Point out each Plasmodium parasite.
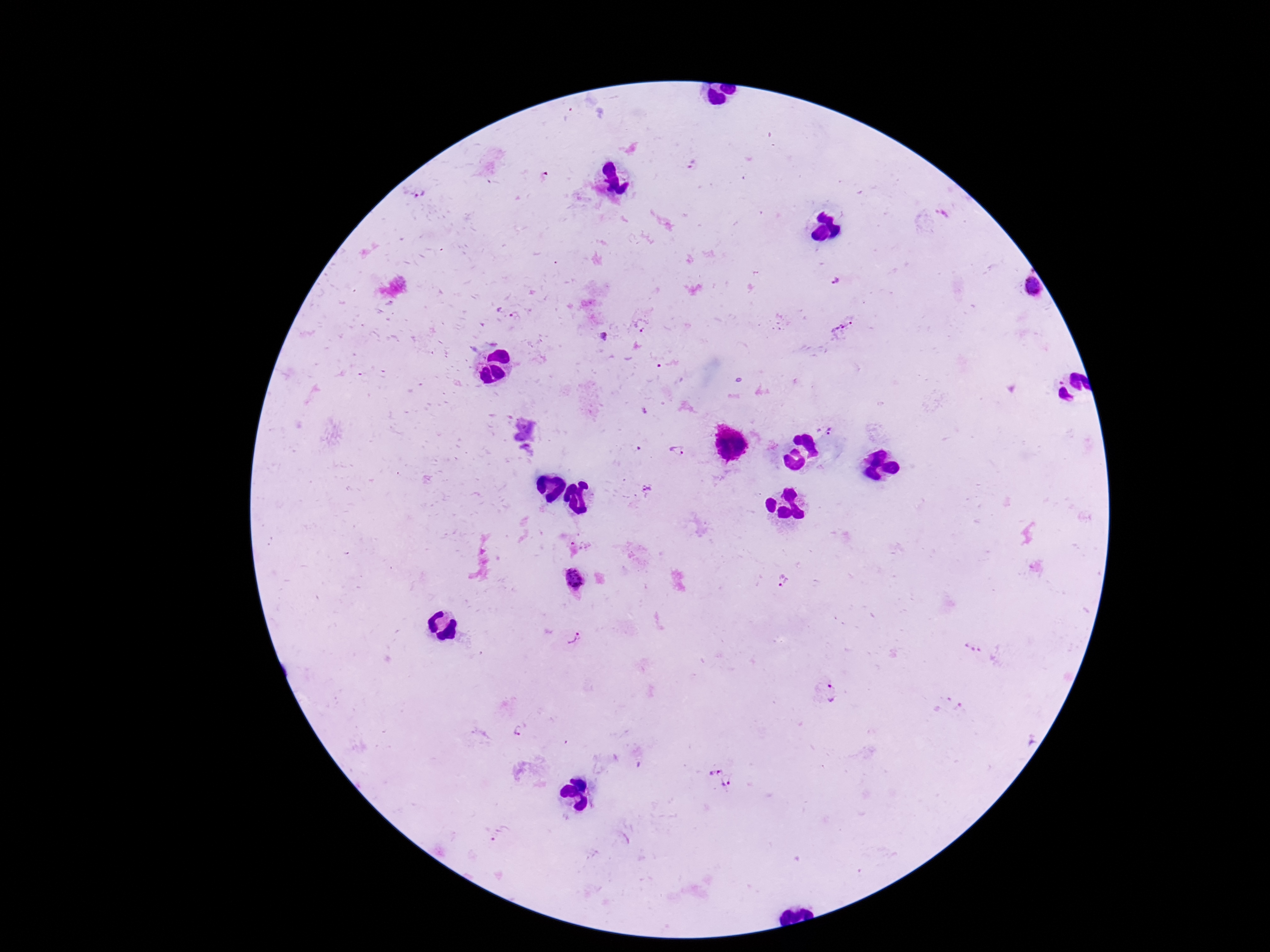
Approximate centers as {x, y} in pixels.
Plasmodium parasites: {1032, 287}, {831, 429}, {679, 451}, {649, 489}, {573, 580}, {783, 583}, {571, 633}, {971, 647}, {834, 692}, {521, 731}, {727, 783}, {500, 836}.

{
  "image_size": "1270×952 pixels",
  "preparation": "thick blood film",
  "stain": "Giemsa",
  "magnification": "100x",
  "capture": "smartphone camera through the microscope eyepiece",
  "field_of_view": "one from this slide",
  "patient_malaria_status": "infected"
}